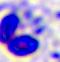

A leukocyte is seen. Photomicrograph. Captured at 400x magnification.